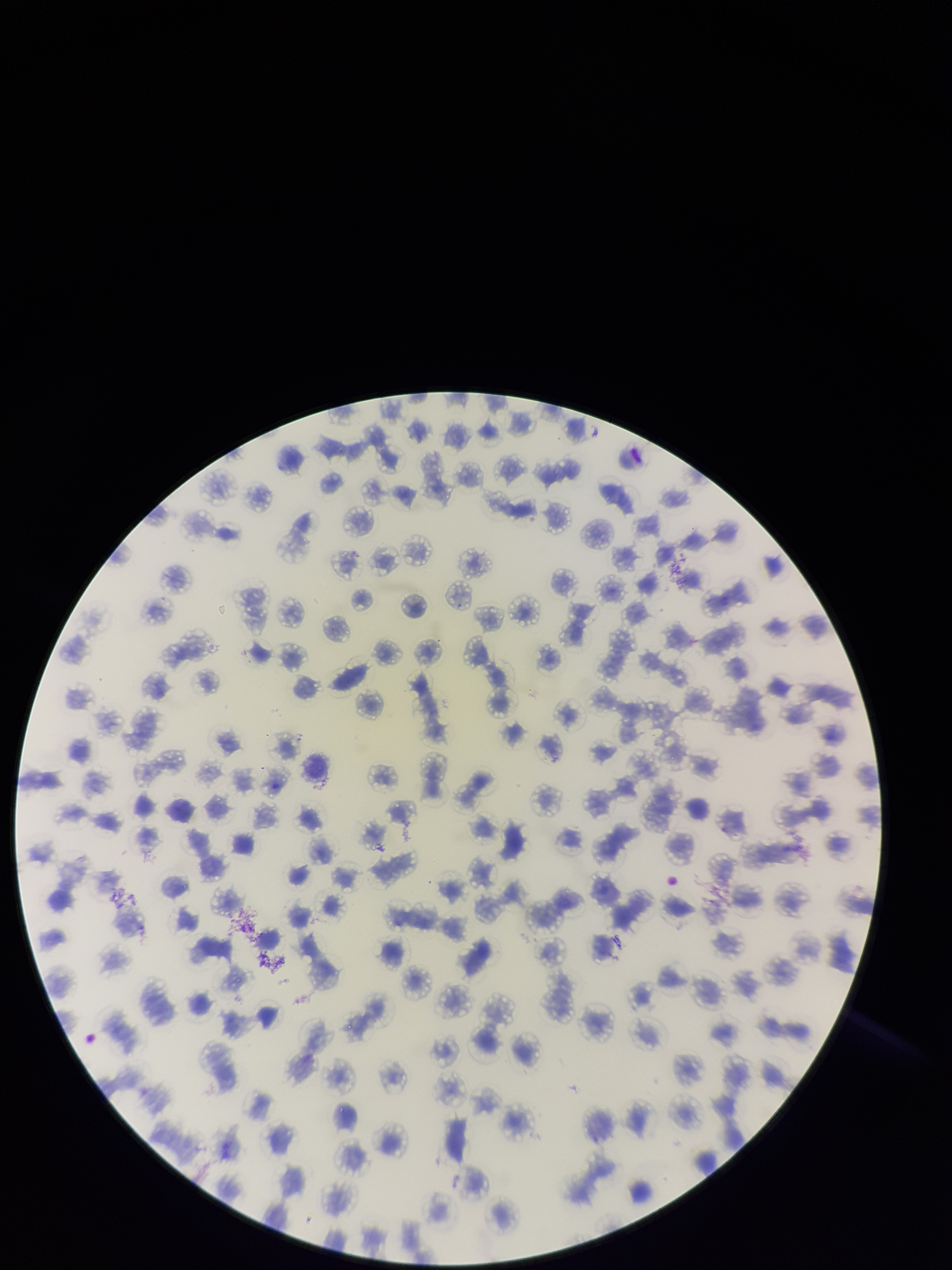
Patient malaria status: positive. Parasitized red blood cells: none seen. Red blood cell count: 212. Parasitized red blood cell count: 0. Preparation: thin blood smear. Species reported for this patient: Plasmodium falciparum. Smartphone photograph taken through the eyepiece of a microscope. Image is 952×1270 pixels. One field from this slide. Giemsa stain.